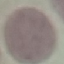

malaria status = uninfected
preparation = thin blood smear
capture = smartphone camera at the microscope eyepiece
stain = Giemsa
image type = cell patch, automatically extracted from a larger field of view and resized to 64 × 64 pixels